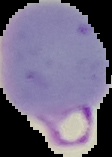

{
  "preparation": "thin blood film",
  "image_size": "112×157 pixels",
  "result": "malaria parasites identified",
  "image_type": "segmented cell region with the area outside set to black"
}